Report the malaria status of this cell.
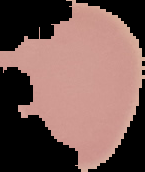
It is uninfected.

Cell region segmented out of the field of view; the surrounding area is masked to black. From a thin blood film. Image is 145×172 pixels.